Describe the morphology of the erythrocytes.
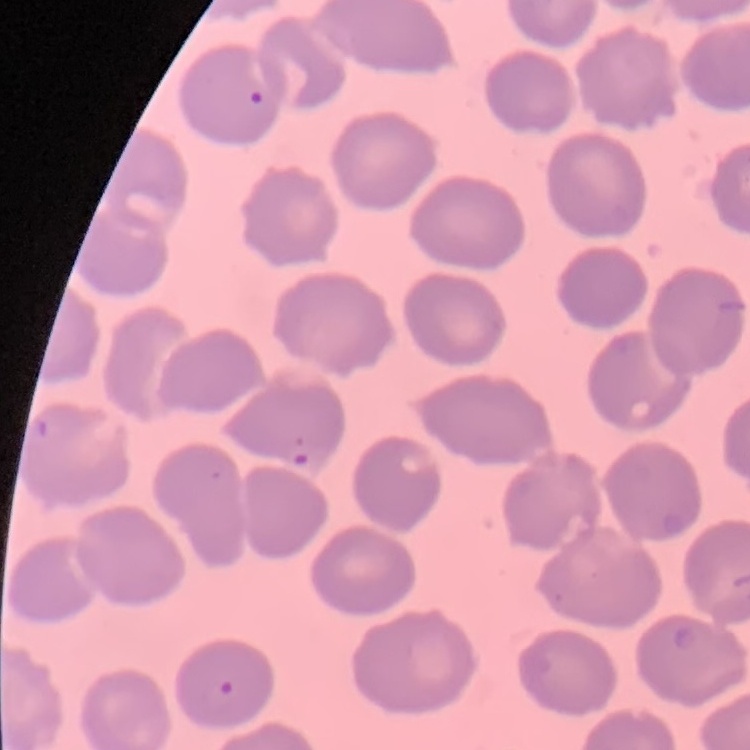
They show no rouleaux formation.

Summary:
  - Preparation: thin blood film
  - Image type: square crop of a larger photomicrograph
  - Stain: Field's or Giemsa